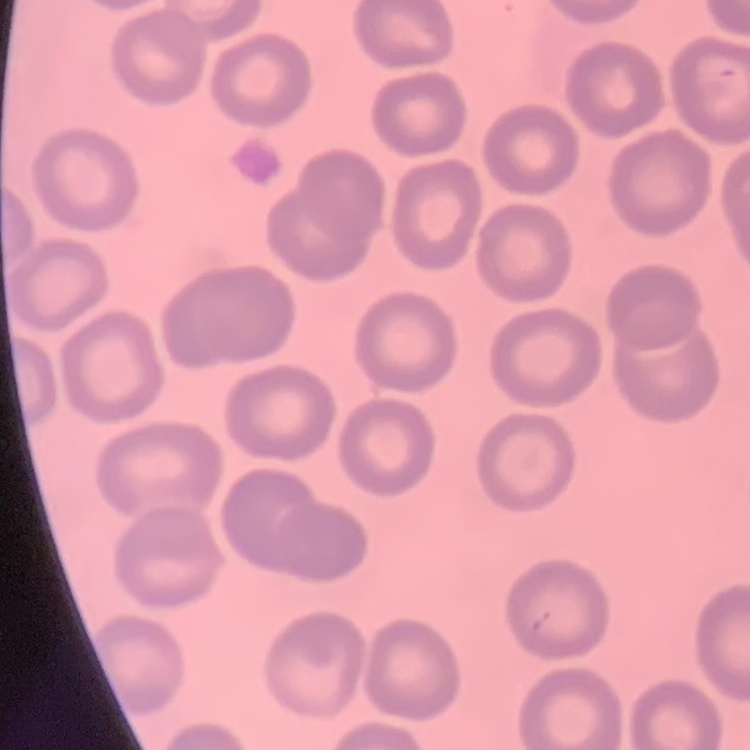
The erythrocytes exhibit no rouleaux formation. Field's or Giemsa stain. One tile cut from a larger photomicrograph. Thin blood smear.